Give the extent of all uninfected red blood cells.
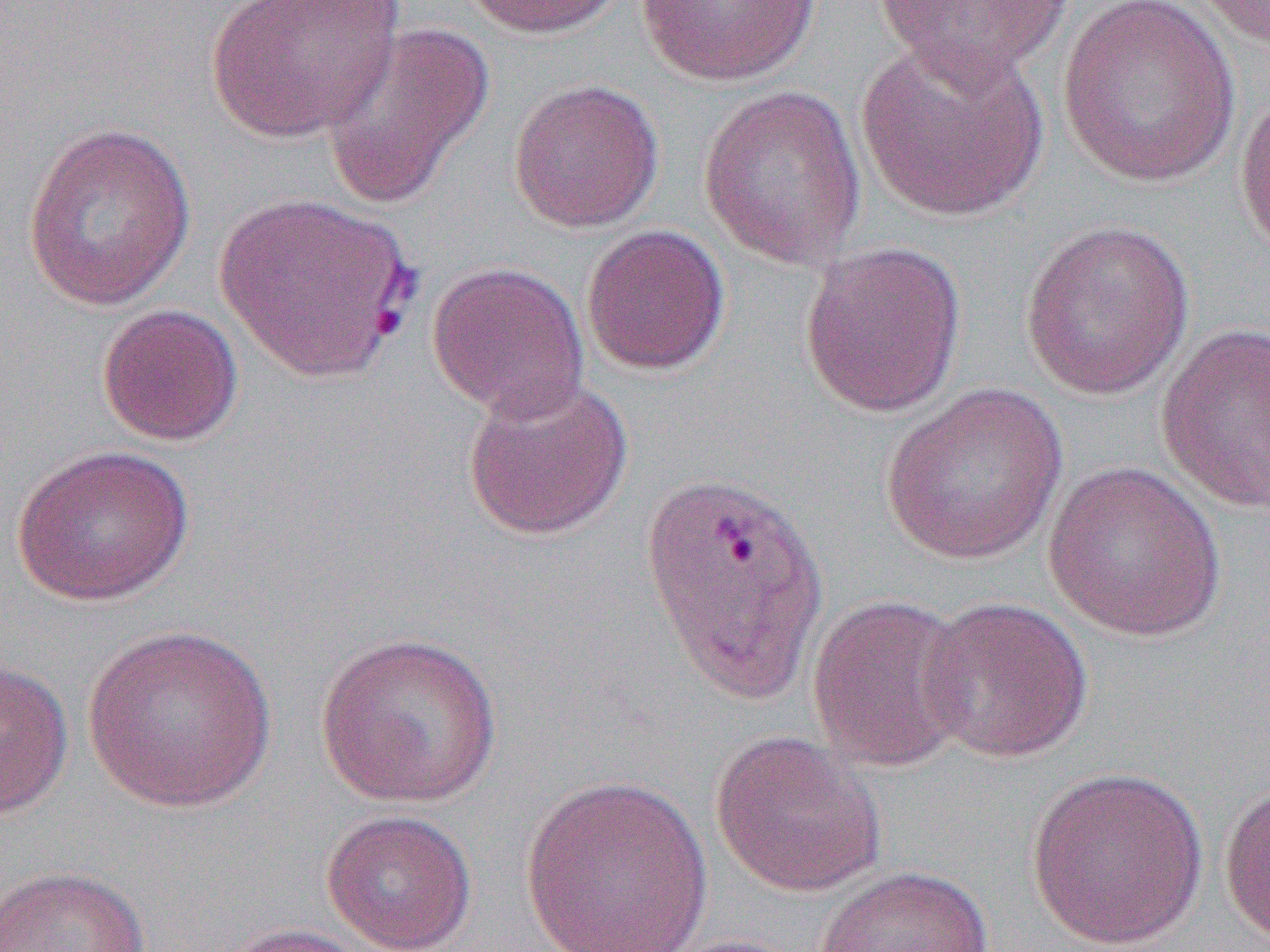
Approximate bounding boxes as named x1/y1/x2/y2 corners in pixels.
Uninfected red blood cells: (x1=206, y1=0, x2=404, y2=143), (x1=459, y1=0, x2=628, y2=39), (x1=636, y1=0, x2=821, y2=87), (x1=872, y1=0, x2=1076, y2=81), (x1=1057, y1=0, x2=1240, y2=188), (x1=1192, y1=0, x2=1270, y2=50), (x1=319, y1=21, x2=495, y2=212), (x1=856, y1=37, x2=1050, y2=223), (x1=508, y1=78, x2=664, y2=233), (x1=698, y1=84, x2=868, y2=270), (x1=1234, y1=87, x2=1270, y2=260), (x1=23, y1=121, x2=197, y2=311), (x1=214, y1=189, x2=418, y2=386), (x1=1020, y1=219, x2=1195, y2=400), (x1=580, y1=225, x2=730, y2=376), (x1=799, y1=240, x2=967, y2=418), (x1=426, y1=261, x2=589, y2=421), (x1=97, y1=304, x2=243, y2=447), (x1=1155, y1=321, x2=1270, y2=515), (x1=461, y1=376, x2=634, y2=542), (x1=879, y1=382, x2=1069, y2=567), (x1=11, y1=444, x2=195, y2=607), (x1=1043, y1=461, x2=1227, y2=641), (x1=806, y1=593, x2=974, y2=773), (x1=917, y1=595, x2=1093, y2=764), (x1=81, y1=623, x2=278, y2=813), (x1=313, y1=630, x2=503, y2=808), (x1=0, y1=657, x2=74, y2=822), (x1=710, y1=730, x2=886, y2=897), (x1=1024, y1=766, x2=1209, y2=950), (x1=518, y1=774, x2=713, y2=952), (x1=1219, y1=779, x2=1270, y2=945), (x1=321, y1=809, x2=478, y2=952), (x1=0, y1=864, x2=149, y2=952), (x1=813, y1=865, x2=993, y2=952), (x1=211, y1=921, x2=373, y2=952), (x1=658, y1=934, x2=810, y2=952).

slide-level diagnosis = Plasmodium vivax
magnification = 1000x
image size = 1270×952 pixels
field of view = one of a larger specimen
preparation = thin blood smear
modality = light microscopy